Report the malaria status of this cell.
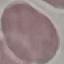
It is uninfected.

Summary:
  - Image type: cell patch, automatically extracted from a larger field of view and resized to 64 × 64 pixels
  - Preparation: thin smear
  - Capture: smartphone through the microscope eyepiece
  - Stain: Giemsa